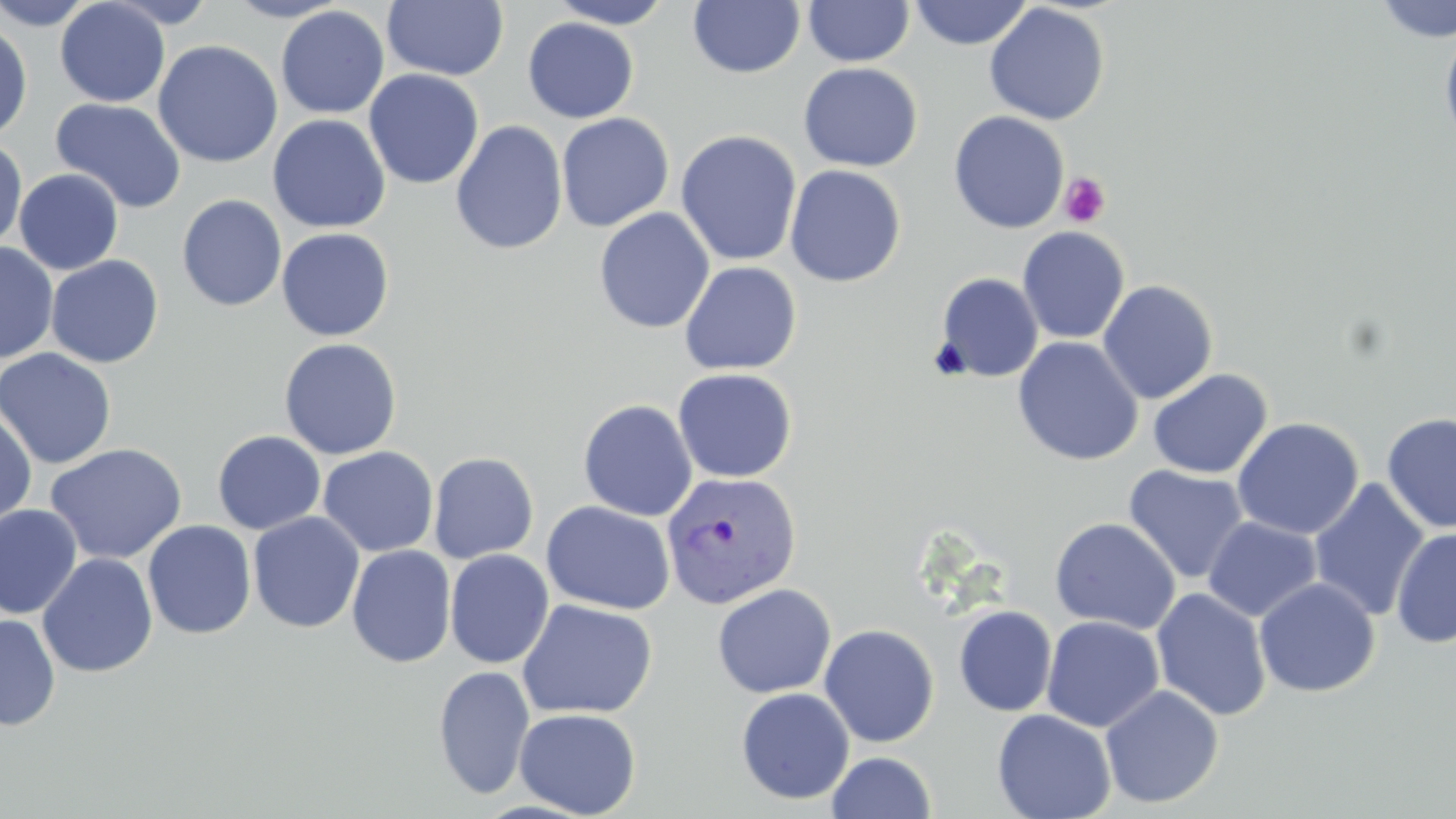

slide_level_diagnosis: Plasmodium vivax
preparation: thin blood film
field_of_view: single
stain: May-Grünwald-Giemsa
modality: optical microscopy
platelet_locations: 'approximate bounding boxes as named x1/y1/x2/y2 corners in pixels: (x1=1059, y1=172, x2=1111, y2=228)'
uninfected_red_blood_cell_locations: 'approximate bounding boxes as named x1/y1/x2/y2 corners in pixels: (x1=0, y1=0, x2=98, y2=30), (x1=55, y1=0, x2=170, y2=107), (x1=103, y1=0, x2=219, y2=28), (x1=225, y1=0, x2=352, y2=22), (x1=382, y1=0, x2=509, y2=81), (x1=546, y1=0, x2=677, y2=28), (x1=803, y1=0, x2=915, y2=67), (x1=1373, y1=0, x2=1456, y2=43), (x1=688, y1=1, x2=805, y2=78), (x1=908, y1=1, x2=1033, y2=50), (x1=984, y1=3, x2=1110, y2=126), (x1=275, y1=6, x2=389, y2=119), (x1=522, y1=17, x2=639, y2=123), (x1=0, y1=19, x2=33, y2=143), (x1=1439, y1=22, x2=1456, y2=154), (x1=153, y1=40, x2=283, y2=168), (x1=798, y1=62, x2=923, y2=172), (x1=363, y1=69, x2=484, y2=190), (x1=84, y1=74, x2=243, y2=199), (x1=50, y1=97, x2=187, y2=214), (x1=948, y1=111, x2=1069, y2=234), (x1=556, y1=113, x2=674, y2=232), (x1=267, y1=114, x2=391, y2=233), (x1=450, y1=120, x2=568, y2=255), (x1=675, y1=129, x2=803, y2=267), (x1=0, y1=136, x2=27, y2=253), (x1=784, y1=164, x2=907, y2=287), (x1=14, y1=168, x2=124, y2=275), (x1=176, y1=194, x2=287, y2=312), (x1=593, y1=208, x2=715, y2=334), (x1=1017, y1=226, x2=1130, y2=344), (x1=276, y1=227, x2=395, y2=341), (x1=0, y1=243, x2=59, y2=364), (x1=45, y1=255, x2=164, y2=369), (x1=679, y1=261, x2=802, y2=376), (x1=935, y1=272, x2=1044, y2=382), (x1=1098, y1=280, x2=1218, y2=404), (x1=278, y1=337, x2=403, y2=460), (x1=1012, y1=337, x2=1143, y2=466), (x1=0, y1=347, x2=117, y2=469), (x1=672, y1=368, x2=797, y2=483), (x1=1147, y1=368, x2=1273, y2=479), (x1=578, y1=398, x2=698, y2=522), (x1=0, y1=410, x2=37, y2=528), (x1=1381, y1=411, x2=1456, y2=534), (x1=1232, y1=417, x2=1363, y2=539), (x1=212, y1=430, x2=326, y2=535), (x1=44, y1=442, x2=188, y2=564), (x1=317, y1=446, x2=439, y2=557), (x1=428, y1=452, x2=539, y2=563), (x1=1122, y1=465, x2=1250, y2=585), (x1=1308, y1=478, x2=1430, y2=621), (x1=541, y1=500, x2=676, y2=614), (x1=0, y1=505, x2=82, y2=619), (x1=247, y1=512, x2=365, y2=633), (x1=1203, y1=516, x2=1322, y2=622), (x1=1050, y1=517, x2=1181, y2=634), (x1=142, y1=520, x2=256, y2=639), (x1=1391, y1=527, x2=1456, y2=649), (x1=346, y1=544, x2=457, y2=668), (x1=444, y1=549, x2=554, y2=669), (x1=37, y1=552, x2=158, y2=678), (x1=1254, y1=577, x2=1381, y2=698), (x1=712, y1=583, x2=836, y2=699), (x1=1151, y1=588, x2=1272, y2=722), (x1=517, y1=599, x2=657, y2=720), (x1=953, y1=605, x2=1057, y2=717), (x1=0, y1=613, x2=61, y2=732), (x1=1041, y1=615, x2=1165, y2=733), (x1=818, y1=623, x2=940, y2=748), (x1=433, y1=665, x2=535, y2=801), (x1=1100, y1=685, x2=1224, y2=808), (x1=735, y1=687, x2=855, y2=805), (x1=513, y1=707, x2=642, y2=818), (x1=992, y1=708, x2=1117, y2=819), (x1=826, y1=751, x2=937, y2=818)'
plasmodium_vivax_infected_red_blood_cell_locations: 'approximate bounding boxes as named x1/y1/x2/y2 corners in pixels: (x1=661, y1=471, x2=801, y2=609)'
magnification: 1000x
image_size: 1456×819 pixels